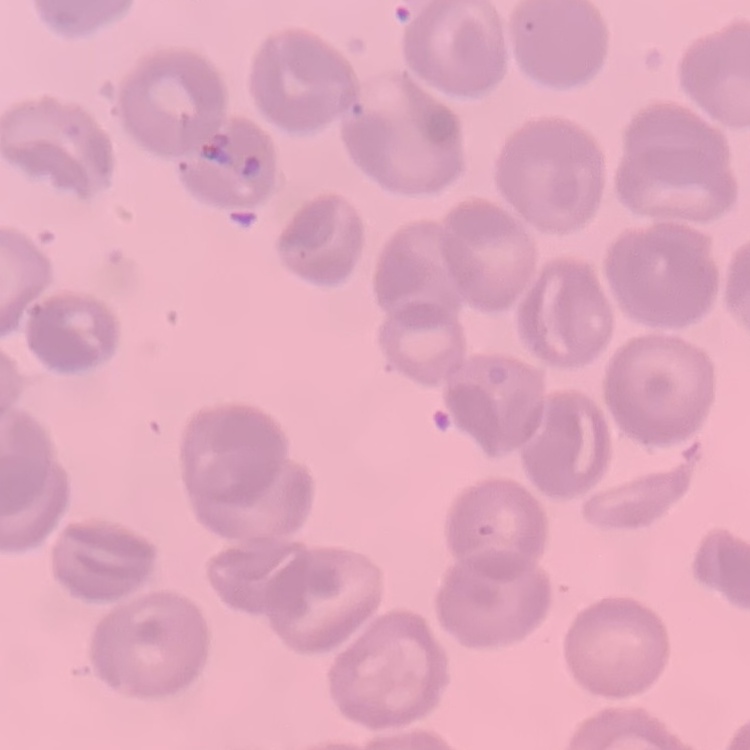

Summary:
  - Erythrocyte morphology: no rouleaux formation
  - Preparation: thin peripheral smear
  - Stain: Field's or Giemsa
  - Image type: one tile cut from a larger photomicrograph